State which cell type is depicted.
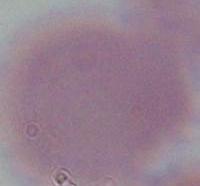
An erythrocyte.

magnification = 1000x
modality = photomicrograph